Assess this cell for malaria.
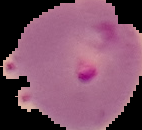

It is parasitized.

preparation = thin blood smear
image size = 142×130 pixels
image type = cell region segmented out of the field of view; surrounding area masked to black